Report the malaria status of this cell.
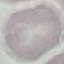
Uninfected.

Thin smear of blood. Giemsa stain. Automatically extracted cell patch, resized to 64 × 64 pixels. Acquired by smartphone through the microscope eyepiece.